Report the malaria status of this cell.
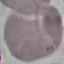

Uninfected.

{
  "capture": "smartphone through the microscope eyepiece",
  "stain": "Giemsa",
  "preparation": "thin smear",
  "image_type": "cell patch, automatically extracted from a larger field of view and resized to 64 × 64 pixels"
}